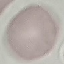
Malaria status: uninfected. Photographed with a smartphone camera at the microscope eyepiece. Thin blood film. Automatically extracted cell patch, resized to 64 × 64 pixels. Giemsa-stained preparation.